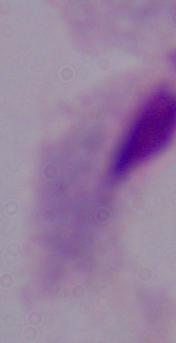
Summary:
  - Identification: trichomonad
  - Magnification: 1000x
  - Modality: photomicrograph